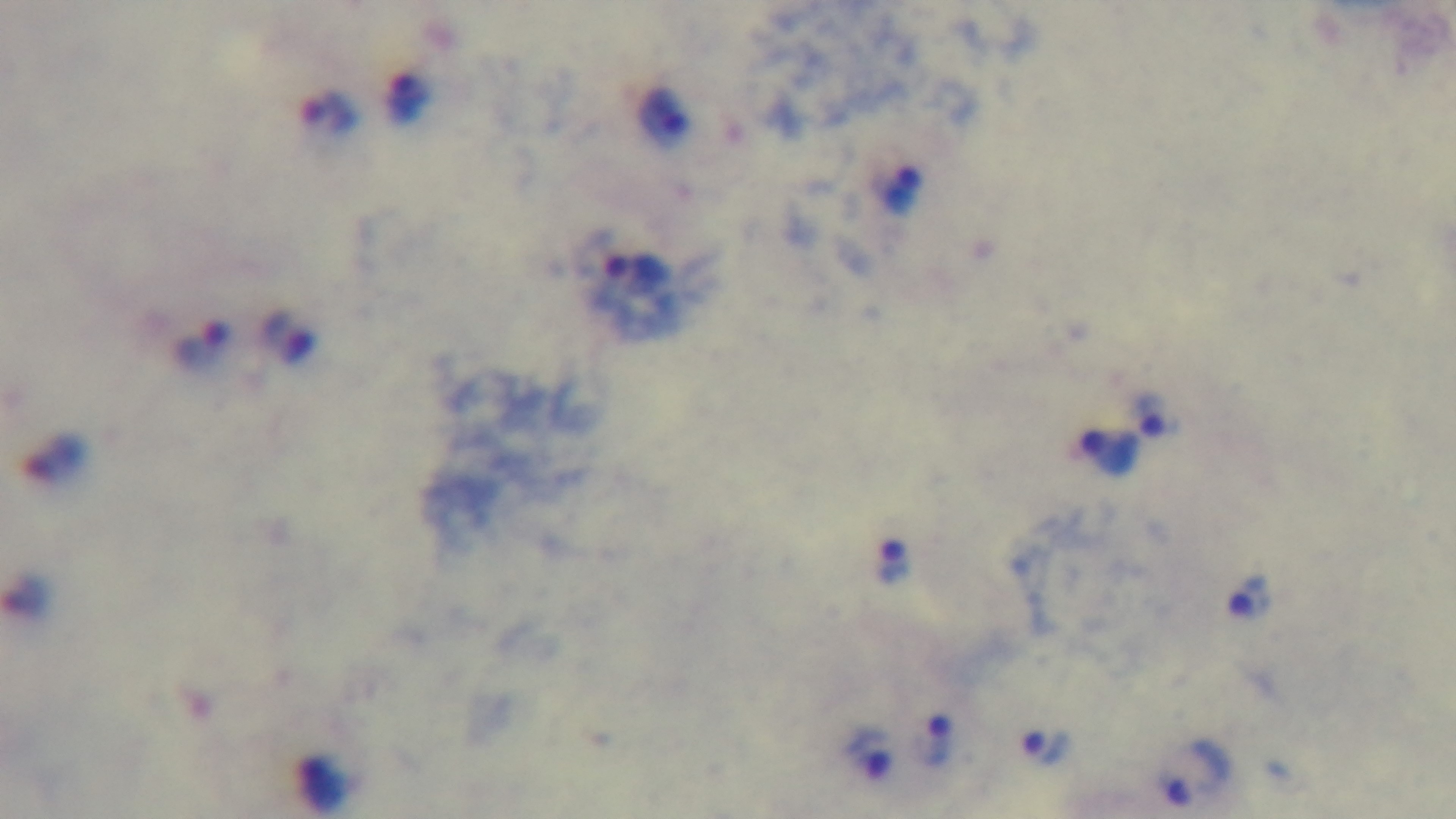 One field from the slide. Oil-immersion objective, 100x. Captured with a mounted 4K digital camera. Preparation: thick smear. Malaria status: positive. Giemsa-stained. Photomicrograph.